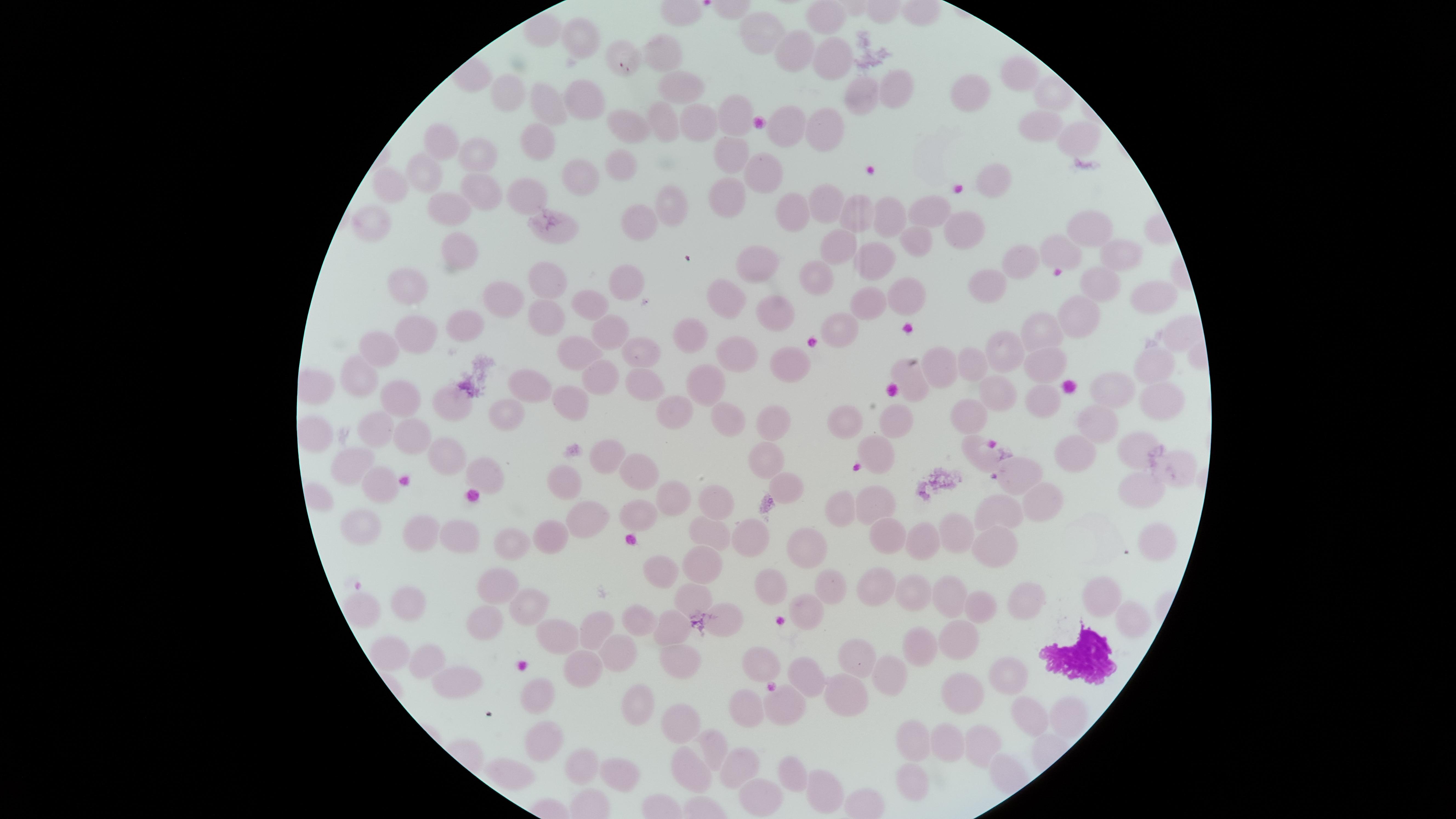
image size = 1456×819 pixels
stain = Giemsa
WBCs = approximate marker points, in pixels from the top-left corner: (x=1075, y=657)
field of view = single
presence = no malaria parasites identified
preparation = thin smear of blood
uninfected RBCs = approximate marker points, in pixels from the top-left corner: (x=829, y=18), (x=771, y=31), (x=576, y=37), (x=796, y=51), (x=663, y=53), (x=830, y=57), (x=623, y=58), (x=1014, y=74), (x=677, y=84), (x=886, y=84), (x=973, y=90), (x=514, y=92), (x=1046, y=92), (x=853, y=96), (x=584, y=98), (x=548, y=103), (x=735, y=112), (x=1033, y=120), (x=661, y=121), (x=692, y=121), (x=787, y=122), (x=825, y=125), (x=627, y=126), (x=1065, y=134), (x=446, y=139), (x=537, y=140), (x=732, y=151), (x=474, y=153), (x=621, y=163), (x=425, y=171), (x=763, y=175), (x=999, y=176), (x=577, y=178), (x=391, y=185), (x=478, y=193), (x=529, y=193), (x=669, y=197), (x=729, y=197), (x=936, y=204), (x=823, y=205), (x=450, y=207), (x=789, y=208), (x=849, y=210), (x=636, y=215), (x=890, y=215), (x=1089, y=222), (x=966, y=225), (x=366, y=229), (x=919, y=237), (x=844, y=247), (x=448, y=249), (x=1062, y=251), (x=1113, y=251), (x=880, y=257), (x=765, y=258), (x=1024, y=262), (x=822, y=275), (x=995, y=276), (x=547, y=278), (x=626, y=278), (x=1095, y=282), (x=410, y=290), (x=729, y=291), (x=510, y=294), (x=1139, y=295), (x=587, y=298), (x=905, y=299), (x=775, y=300), (x=871, y=301), (x=546, y=312), (x=1081, y=315), (x=463, y=323), (x=1045, y=323), (x=606, y=329), (x=697, y=329), (x=837, y=329), (x=415, y=333), (x=386, y=341), (x=1002, y=347), (x=576, y=352), (x=742, y=352), (x=640, y=354), (x=791, y=359), (x=1042, y=361), (x=943, y=362), (x=970, y=363), (x=1156, y=364), (x=599, y=372), (x=358, y=377), (x=645, y=377), (x=531, y=381), (x=913, y=382), (x=707, y=383), (x=996, y=385), (x=1105, y=387), (x=395, y=389), (x=1035, y=394), (x=573, y=395), (x=460, y=397), (x=1165, y=399), (x=508, y=404), (x=674, y=407), (x=968, y=410), (x=896, y=414), (x=1104, y=414), (x=834, y=417), (x=727, y=422), (x=777, y=424), (x=370, y=425), (x=408, y=428), (x=312, y=432), (x=1129, y=441), (x=979, y=448), (x=879, y=450), (x=1077, y=455), (x=443, y=457), (x=761, y=457), (x=608, y=458), (x=354, y=461), (x=1176, y=467), (x=644, y=470), (x=1016, y=471), (x=487, y=472), (x=381, y=486), (x=786, y=486), (x=562, y=487), (x=1038, y=493), (x=1139, y=493), (x=873, y=497), (x=716, y=498), (x=668, y=500), (x=841, y=506), (x=997, y=509), (x=634, y=515), (x=584, y=518), (x=359, y=528), (x=417, y=529), (x=551, y=532), (x=883, y=533), (x=959, y=533), (x=710, y=535), (x=457, y=536), (x=749, y=540), (x=918, y=541), (x=1154, y=542), (x=991, y=546), (x=801, y=547), (x=515, y=552), (x=702, y=559), (x=663, y=567), (x=498, y=580), (x=874, y=585), (x=824, y=586), (x=771, y=587), (x=689, y=591), (x=957, y=594), (x=905, y=595), (x=1100, y=597), (x=1035, y=600), (x=409, y=602), (x=984, y=602), (x=364, y=606), (x=525, y=608), (x=806, y=612), (x=728, y=613), (x=491, y=617), (x=645, y=621), (x=672, y=622), (x=1130, y=622), (x=564, y=634), (x=598, y=634), (x=956, y=634), (x=908, y=643), (x=393, y=648), (x=614, y=652), (x=861, y=653), (x=433, y=659), (x=677, y=659), (x=582, y=665), (x=765, y=666), (x=806, y=670), (x=886, y=671), (x=455, y=674), (x=1016, y=678), (x=540, y=687), (x=846, y=688), (x=962, y=696), (x=633, y=703), (x=745, y=706), (x=782, y=706), (x=1018, y=710), (x=1067, y=715), (x=680, y=719), (x=911, y=736), (x=536, y=738), (x=990, y=739), (x=717, y=745), (x=951, y=748), (x=581, y=761), (x=741, y=761), (x=689, y=766), (x=796, y=768), (x=516, y=773), (x=609, y=775), (x=912, y=776), (x=819, y=781), (x=760, y=790)
capture = smartphone photograph through the microscope eyepiece
visible region = circular